Name the parasite shown.
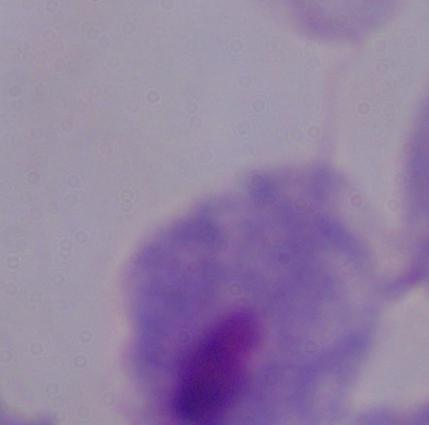

A trichomonad.

Summary:
  - Magnification: 1000x
  - Modality: photomicrograph